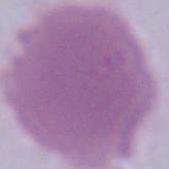

Summary:
  - Identification: red blood cell
  - Modality: micrograph
  - Magnification: 1000x